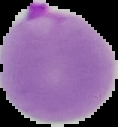
Image is 118×127 pixels. Result: Plasmodium parasites identified. Segmented cell region on a black background. From a thin blood film.